Report the malaria status of this cell.
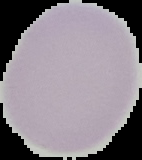
Uninfected.

Segmented cell region on a black background. Image is 142×160 pixels. From a thin blood smear.